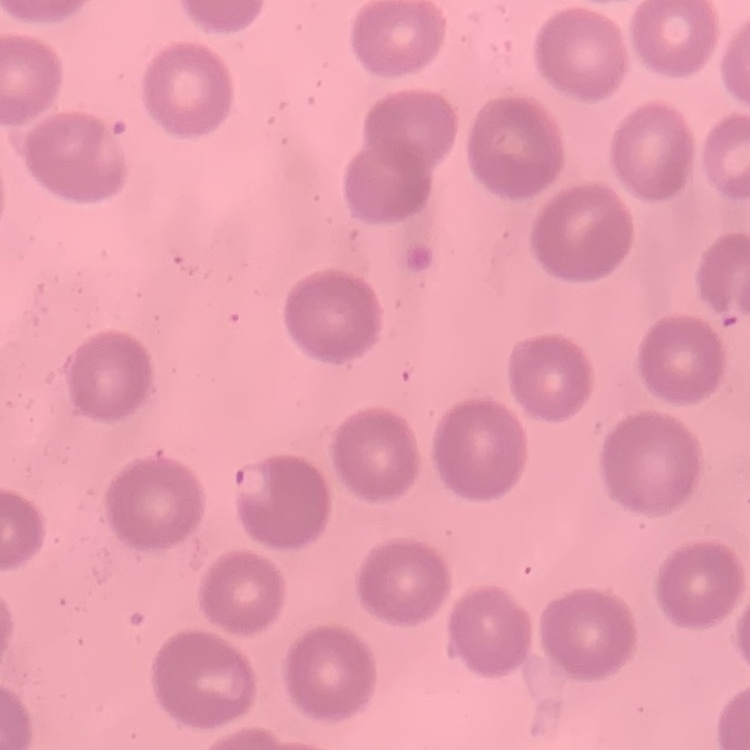

Summary:
  - Erythrocyte morphology: no rouleaux formation
  - Image type: square crop of a larger photomicrograph
  - Preparation: thin blood smear
  - Stain: Field's or Giemsa